Point out each malaria parasite.
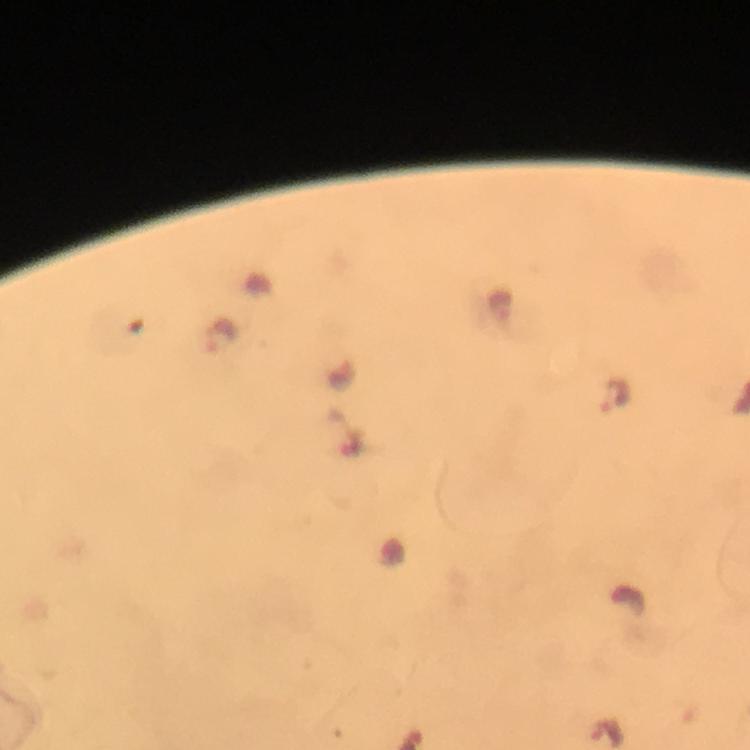
Approximate centers as [x, y] in pixels.
Malaria parasites: [220, 337], [615, 396].

Image is 750×750 pixels. Giemsa-stained preparation. From a malaria diagnostic workup. Photographed with a smartphone mounted on the microscope. Thick blood film. Immersion oil was used. A crop from one field of view. At 100x magnification.